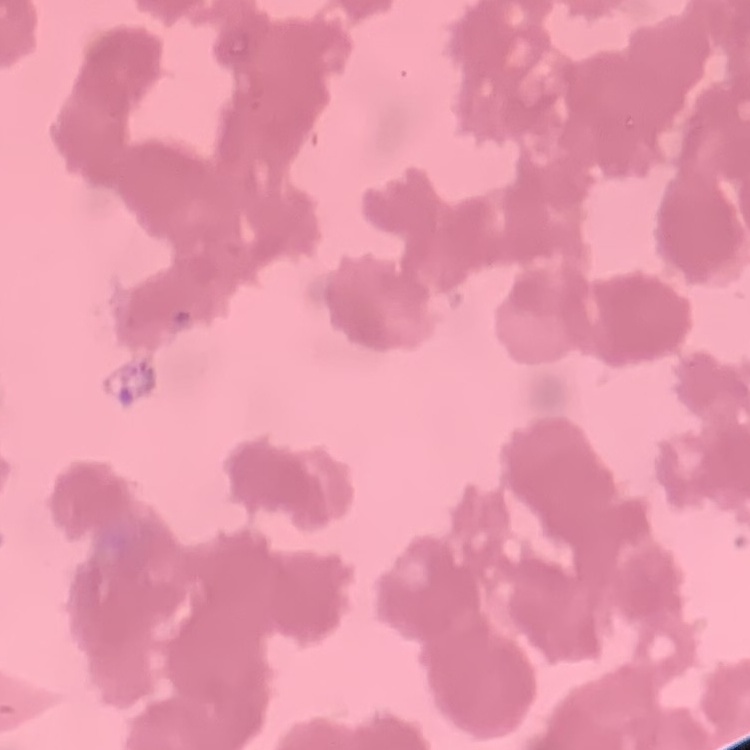

erythrocyte morphology = rouleaux formation
preparation = thin blood film
stain = Field's or Giemsa
image type = square crop of a larger photomicrograph